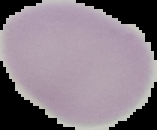
image type = segmented cell region on a black background
result = no Plasmodium parasites seen
image size = 157×130 pixels
preparation = thin blood smear